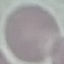 Result: no malaria parasites detected. Giemsa stain. Automatically extracted cell patch, resized to 64 × 64 pixels. Photographed with a smartphone camera at the microscope eyepiece. Thin blood smear.